Name the blood parasite species.
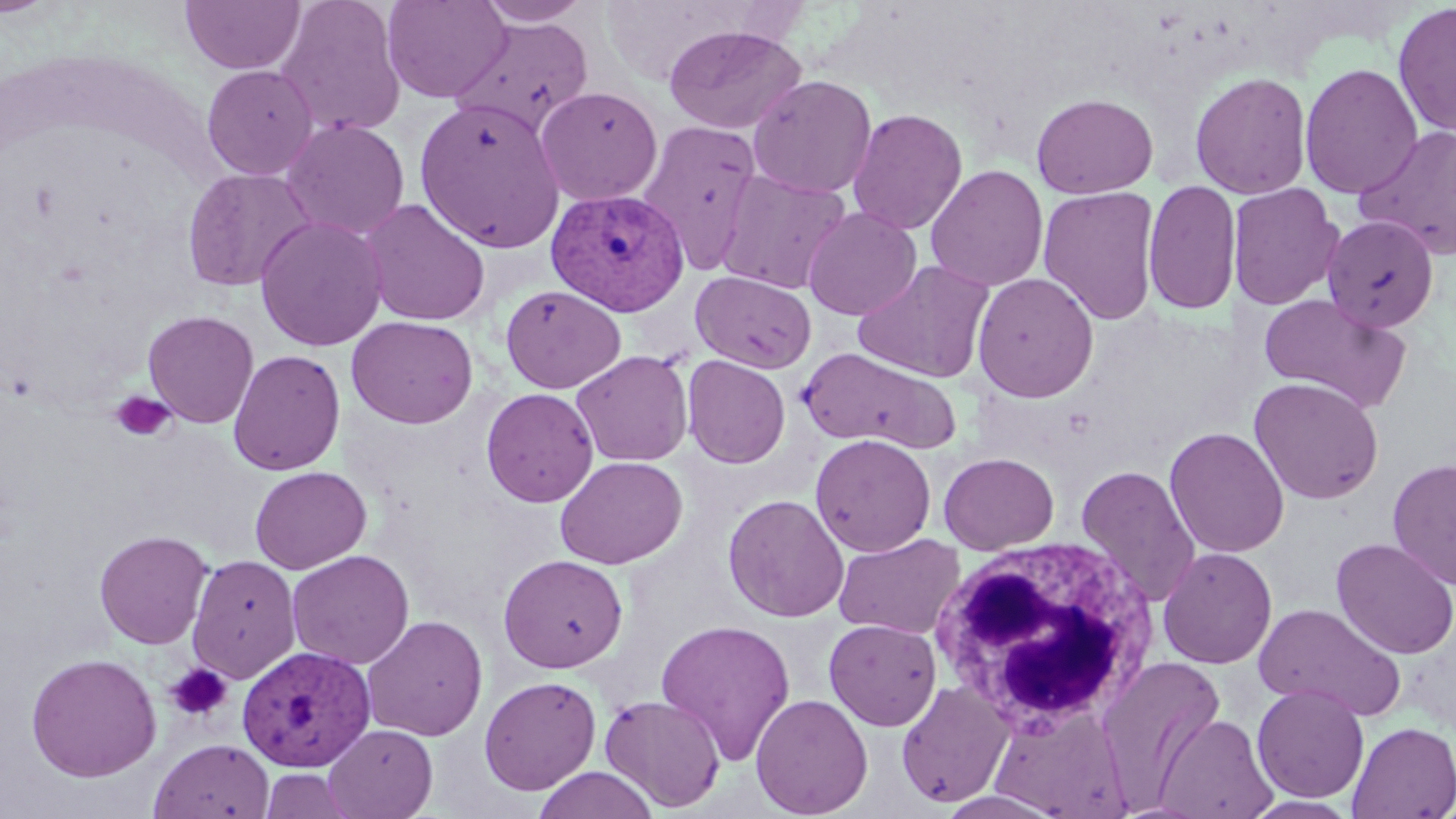
Plasmodium vivax.

image_size: 1456×819 pixels
plasmodium_vivax_infected_red_blood_cell_locations: 'approximate bounding boxes as (x1,y1)-(x2,y2) corner pairs in pixels: (545,187)-(690,316), (234,644)-(375,770)'
modality: optical microscopy
uninfected_red_blood_cell_locations: 'approximate bounding boxes as (x1,y1)-(x2,y2) corner pairs in pixels: (180,0)-(305,75), (275,0)-(406,138), (382,0)-(511,103), (475,1)-(593,27), (1392,2)-(1456,138), (450,15)-(594,137), (663,25)-(807,134), (1299,63)-(1423,200), (202,64)-(318,180), (1190,71)-(1313,199), (747,75)-(877,198), (535,85)-(663,206), (1031,92)-(1158,199), (414,99)-(566,253), (848,108)-(967,234), (280,118)-(410,240), (637,119)-(764,273), (1356,124)-(1456,259), (925,164)-(1049,291), (181,168)-(316,292), (715,169)-(851,294), (1143,178)-(1242,316), (1227,182)-(1344,310), (1038,186)-(1161,326), (361,199)-(491,326), (803,206)-(921,320), (1322,214)-(1439,333), (255,216)-(388,351), (853,259)-(995,383), (690,270)-(816,373), (971,272)-(1099,403), (821,273)-(980,448), (500,284)-(625,394), (1257,293)-(1411,413), (143,310)-(259,428), (347,315)-(478,428), (799,348)-(960,452), (228,350)-(345,475), (571,350)-(693,466), (682,355)-(790,468), (1248,377)-(1384,505), (480,387)-(599,507), (1164,426)-(1289,558), (810,433)-(936,557), (939,452)-(1059,554), (554,455)-(688,570), (1387,457)-(1456,589), (1076,464)-(1200,606), (250,466)-(372,573), (722,493)-(849,622), (94,530)-(212,649), (833,533)-(965,640), (1331,538)-(1456,660), (1158,547)-(1277,669), (287,550)-(414,669), (498,553)-(628,672), (187,554)-(301,682), (1253,602)-(1406,721), (361,615)-(488,741), (655,618)-(796,765), (823,618)-(942,731), (25,652)-(162,782), (1096,655)-(1225,804), (479,676)-(601,795), (895,680)-(1016,808), (1252,683)-(1369,803), (600,694)-(726,812), (751,694)-(873,818), (989,701)-(1132,817), (1154,713)-(1277,818), (1347,721)-(1456,818), (323,723)-(438,818), (149,737)-(274,819), (532,767)-(660,819), (258,768)-(358,819), (1242,795)-(1362,818)'
field_of_view: single
magnification: 1000x
preparation: thin blood film
platelet_locations: 'approximate bounding boxes as (x1,y1)-(x2,y2) corner pairs in pixels: (109,391)-(177,443), (165,663)-(233,723)'
white_blood_cell_locations: 'approximate bounding boxes as (x1,y1)-(x2,y2) corner pairs in pixels: (929,535)-(1161,734)'
stain: May-Grünwald-Giemsa